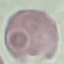

Result: no malaria parasites seen. Thin smear of blood. Giemsa-stained preparation. Photographed with a smartphone camera at the microscope eyepiece. Cell patch, automatically extracted from a larger field of view and resized to 64 × 64 pixels.